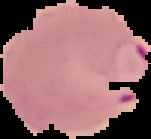

Summary:
  - Malaria status: parasitized
  - Image type: cell region segmented out of the field of view; surrounding area masked to black
  - Preparation: thin blood film
  - Image size: 151×139 pixels